Classify this cell by malaria status.
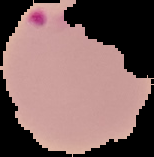
Parasitized.

Image is 154×157 pixels. Segmented cell region on a black background. From a thin blood film.